Assess this cell for malaria.
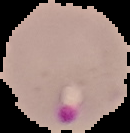
It is parasitized.

Image is 130×133 pixels. From a thin blood smear. Segmented cell region on a black background.